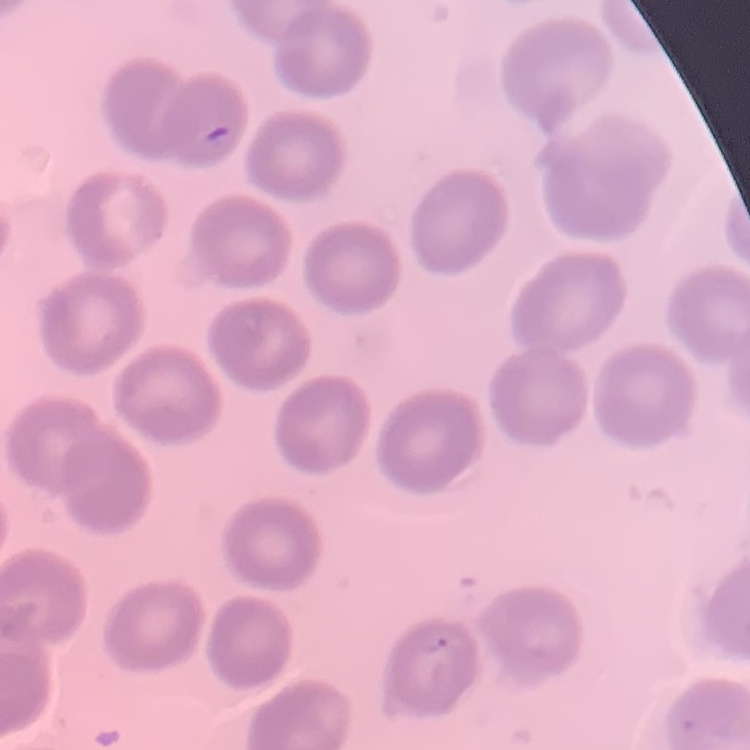

Summary:
  - Erythrocyte morphology: no rouleaux formation
  - Image type: square crop of a larger photomicrograph
  - Preparation: thin blood film
  - Stain: Field's or Giemsa